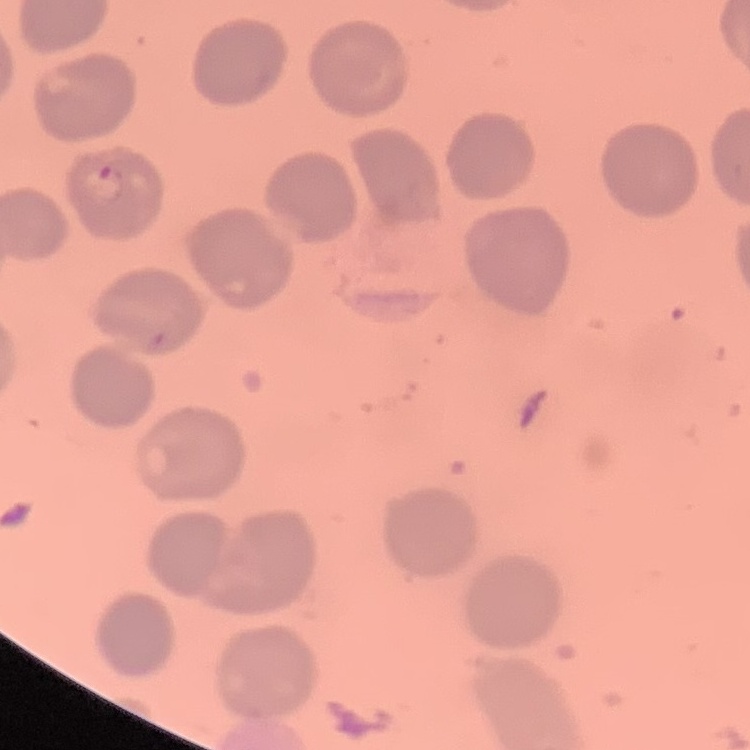
{
  "red_blood_cell_morphology": "no rouleaux formation",
  "image_type": "square crop of a larger photomicrograph",
  "stain": "Field's or Giemsa",
  "preparation": "thin blood film"
}